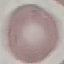

Summary:
  - Malaria status: uninfected
  - Capture: smartphone through the microscope eyepiece
  - Preparation: thin smear
  - Image type: cell patch, automatically extracted from a larger field of view and resized to 64 × 64 pixels
  - Stain: Giemsa